Identify the blood parasite species.
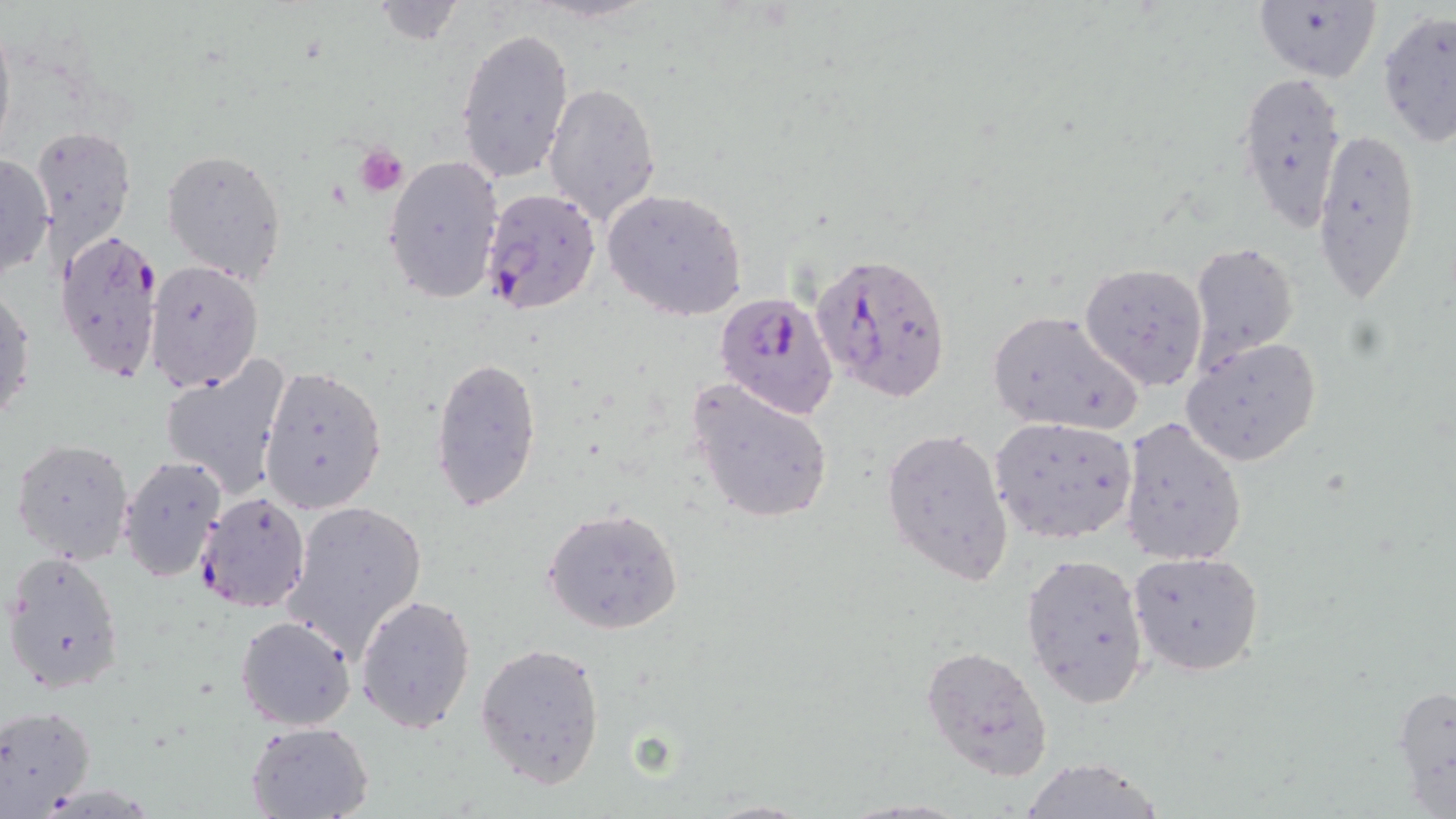
Plasmodium falciparum.

Approximate bounding boxes as (x1, y1, x2, y2) in pixels. Plasmodium falciparum-infected red blood cell locations: (479, 186, 601, 316), (55, 228, 163, 385), (810, 248, 953, 403), (713, 290, 839, 421), (194, 489, 311, 613). Uninfected red blood cell locations: (368, 0, 468, 46), (1251, 1, 1382, 84), (1376, 9, 1455, 147), (0, 13, 15, 163), (455, 27, 576, 184), (1235, 69, 1348, 234), (543, 82, 662, 225), (32, 123, 136, 261), (1310, 127, 1421, 302), (162, 148, 288, 283), (0, 152, 52, 283), (382, 154, 504, 306), (603, 188, 749, 322), (1190, 242, 1301, 368), (146, 260, 264, 395), (1080, 263, 1209, 391), (1, 286, 35, 429), (986, 308, 1143, 435), (1180, 337, 1324, 467), (430, 352, 543, 512), (159, 356, 292, 498), (258, 364, 387, 515), (688, 378, 836, 525), (989, 416, 1140, 544), (1118, 416, 1248, 566), (880, 426, 1015, 587), (11, 437, 135, 566), (118, 454, 228, 584), (279, 498, 427, 662), (542, 506, 683, 634), (1020, 551, 1150, 710), (1127, 551, 1265, 676), (3, 552, 125, 695), (355, 594, 476, 733), (234, 615, 357, 731), (474, 641, 607, 789), (920, 644, 1054, 781), (1391, 679, 1456, 814), (0, 704, 95, 819), (245, 720, 373, 818), (1018, 757, 1167, 819), (698, 799, 817, 819). Platelet locations: (355, 142, 409, 196). One field of a larger specimen. Image is 1456×819 pixels. 1000x magnification. Light microscopy. May-Grünwald-Giemsa stain. Thin blood smear.